Report the malaria status of this cell.
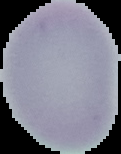

Uninfected.

Summary:
  - Image size: 121×154 pixels
  - Preparation: thin blood smear
  - Image type: segmented cell region on a black background